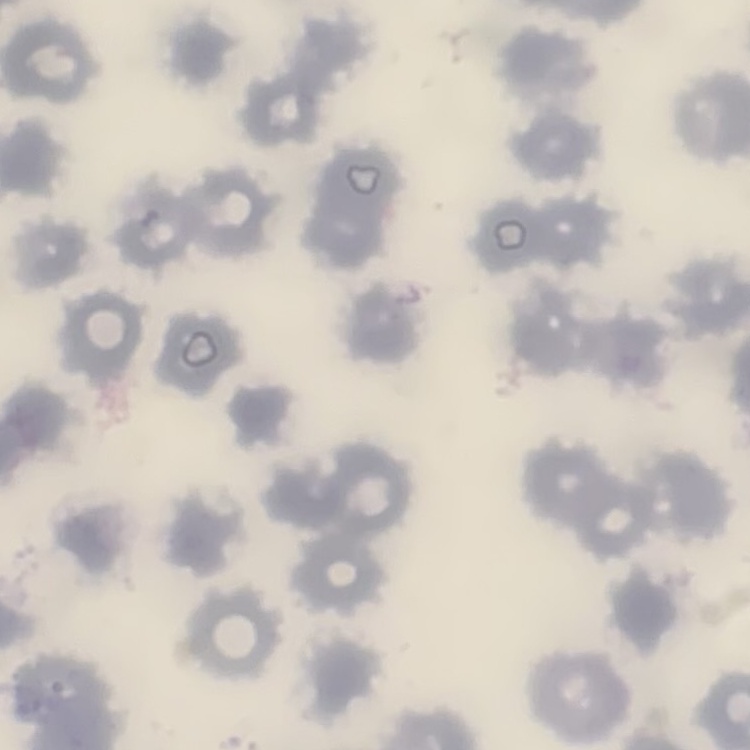

red blood cell morphology = no rouleaux formation
image type = one tile cut from a larger photomicrograph
preparation = thin blood smear
stain = Field's or Giemsa